Locate every blood parasite and identify its species.
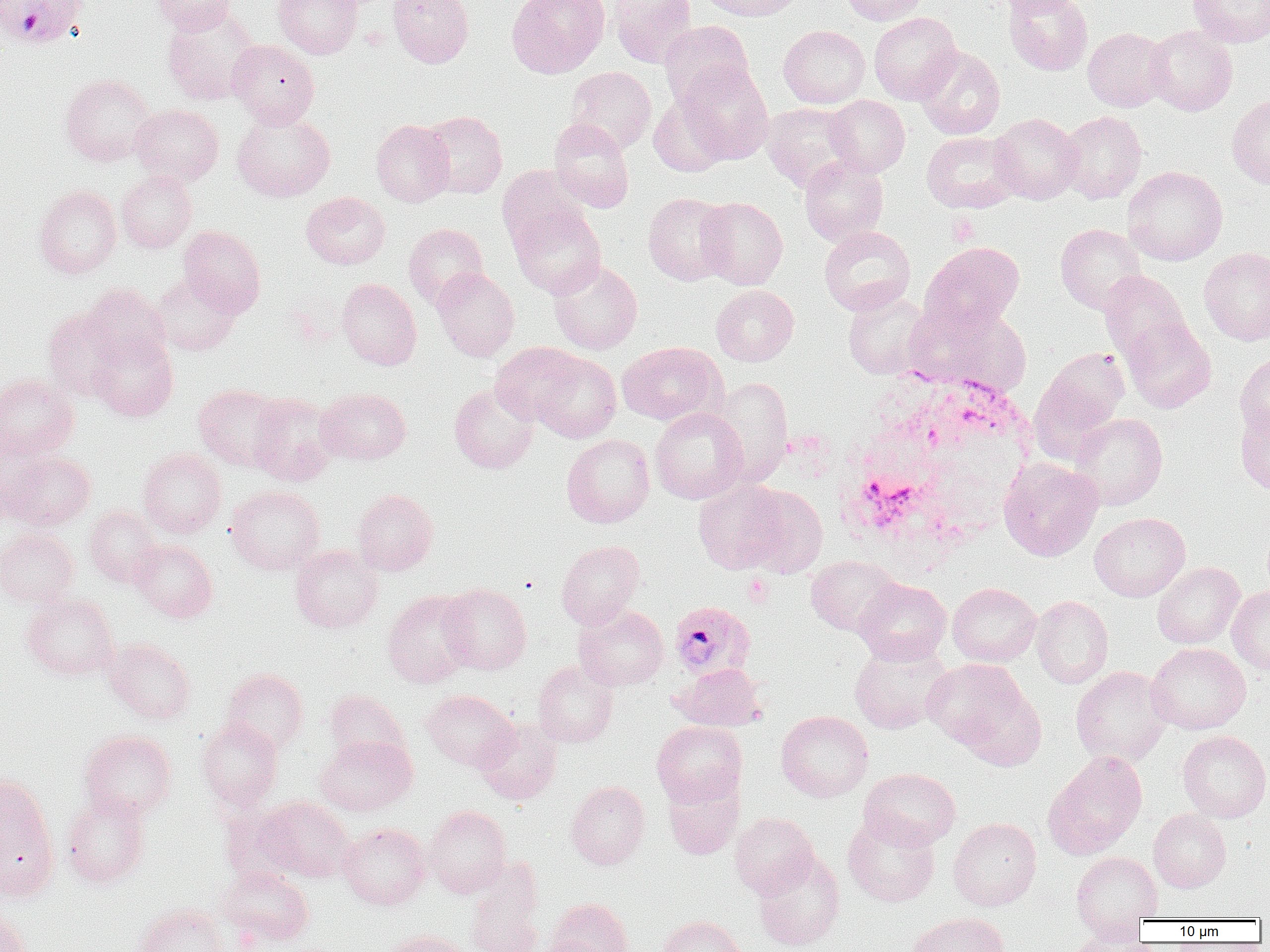
Approximate bounding boxes as (x1, y1, x2, y2) in pixels.
Plasmodium falciparum-infected red blood cells: (1, 0, 89, 49), (668, 601, 755, 681).
No Plasmodium ovale, Plasmodium malariae, Plasmodium vivax, Babesia divergens, or Trypanosoma brucei observed.

slide-level diagnosis = Plasmodium falciparum
platelet locations = approximate bounding boxes as (x1, y1, x2, y2) in pixels: (947, 214, 980, 245), (743, 574, 773, 606)
uninfected red blood cell locations = approximate bounding boxes as (x1, y1, x2, y2) in pixels: (152, 0, 236, 35), (273, 0, 362, 59), (388, 0, 474, 68), (507, 0, 610, 78), (609, 0, 697, 68), (696, 0, 805, 22), (840, 0, 928, 25), (990, 0, 1085, 16), (1003, 0, 1093, 76), (1187, 0, 1270, 47), (162, 6, 261, 106), (869, 12, 961, 104), (659, 20, 754, 109), (778, 25, 870, 109), (1146, 25, 1237, 116), (1083, 27, 1172, 111), (227, 39, 319, 128), (915, 46, 1005, 140), (673, 63, 774, 165), (565, 67, 656, 153), (59, 73, 156, 167), (1227, 93, 1270, 189), (824, 95, 910, 177), (648, 96, 736, 177), (761, 103, 860, 192), (131, 104, 223, 186), (231, 110, 335, 202), (420, 110, 507, 198), (1057, 111, 1147, 204), (989, 113, 1082, 204), (548, 118, 635, 212), (371, 119, 454, 206), (921, 132, 1020, 213), (799, 155, 888, 246), (497, 165, 589, 253), (1123, 166, 1227, 266), (116, 170, 196, 253), (34, 185, 121, 279), (300, 191, 390, 270), (643, 193, 734, 285), (696, 197, 788, 290), (510, 204, 606, 298), (403, 223, 488, 308), (1055, 224, 1146, 315), (819, 225, 915, 315), (178, 226, 266, 316), (920, 241, 1024, 332), (1199, 247, 1270, 346), (548, 259, 642, 354), (432, 268, 519, 360), (1099, 271, 1192, 367), (151, 274, 240, 356), (337, 278, 421, 370), (82, 283, 171, 369), (711, 285, 799, 366), (843, 291, 932, 379), (916, 305, 1033, 396), (43, 309, 126, 400), (1121, 317, 1216, 414), (88, 331, 178, 421), (617, 341, 726, 425), (490, 342, 585, 426), (1029, 349, 1130, 460), (531, 351, 621, 443), (1235, 352, 1270, 437), (0, 374, 79, 460), (712, 377, 793, 484), (193, 384, 286, 471), (449, 384, 539, 473), (316, 388, 411, 464), (246, 393, 338, 486), (1235, 404, 1270, 498), (649, 407, 747, 504), (1070, 413, 1168, 510), (561, 434, 655, 528), (0, 438, 41, 526), (137, 448, 227, 538), (3, 451, 95, 531), (998, 458, 1103, 561), (693, 478, 790, 574), (226, 485, 325, 575), (740, 485, 828, 577), (351, 489, 438, 575), (84, 505, 162, 587), (1090, 512, 1190, 601), (0, 529, 79, 607), (130, 538, 217, 622), (556, 540, 645, 629), (290, 545, 383, 633), (806, 555, 903, 636), (1152, 562, 1245, 649), (853, 578, 952, 665), (947, 582, 1041, 667), (440, 583, 532, 675), (1227, 586, 1270, 673), (383, 590, 477, 687), (22, 592, 119, 680), (1031, 595, 1114, 688), (574, 605, 669, 690), (103, 637, 196, 724), (849, 640, 953, 735), (1146, 643, 1251, 734), (924, 659, 1031, 753), (533, 660, 619, 747), (671, 663, 766, 731), (1071, 665, 1172, 765), (221, 668, 308, 754), (954, 681, 1047, 771), (324, 690, 409, 763), (422, 690, 518, 772), (776, 710, 873, 802), (197, 717, 282, 809), (475, 719, 562, 805), (651, 721, 747, 807), (79, 730, 176, 820), (1177, 731, 1270, 822), (315, 735, 417, 815), (1044, 751, 1147, 859), (859, 767, 961, 849), (0, 774, 59, 898), (662, 775, 743, 860), (566, 780, 649, 870), (61, 791, 151, 889), (258, 796, 354, 883), (423, 805, 511, 897), (1148, 807, 1231, 892), (730, 812, 819, 899), (842, 813, 940, 907), (948, 817, 1041, 910), (339, 822, 431, 910), (1071, 851, 1163, 931), (753, 852, 845, 951), (465, 860, 544, 952), (217, 865, 315, 948), (548, 897, 633, 952), (133, 903, 229, 952), (0, 907, 32, 952), (907, 911, 1009, 952), (658, 915, 747, 952), (382, 929, 472, 952), (1059, 929, 1149, 952), (539, 936, 608, 952)
magnification = 1000x
white blood cell locations = approximate bounding boxes as (x1, y1, x2, y2) in pixels: (834, 370, 1037, 561)
preparation = thin blood film
field of view = one of a larger specimen
modality = optical microscopy
image size = 1270×952 pixels